Locate every blood parasite and identify its species.
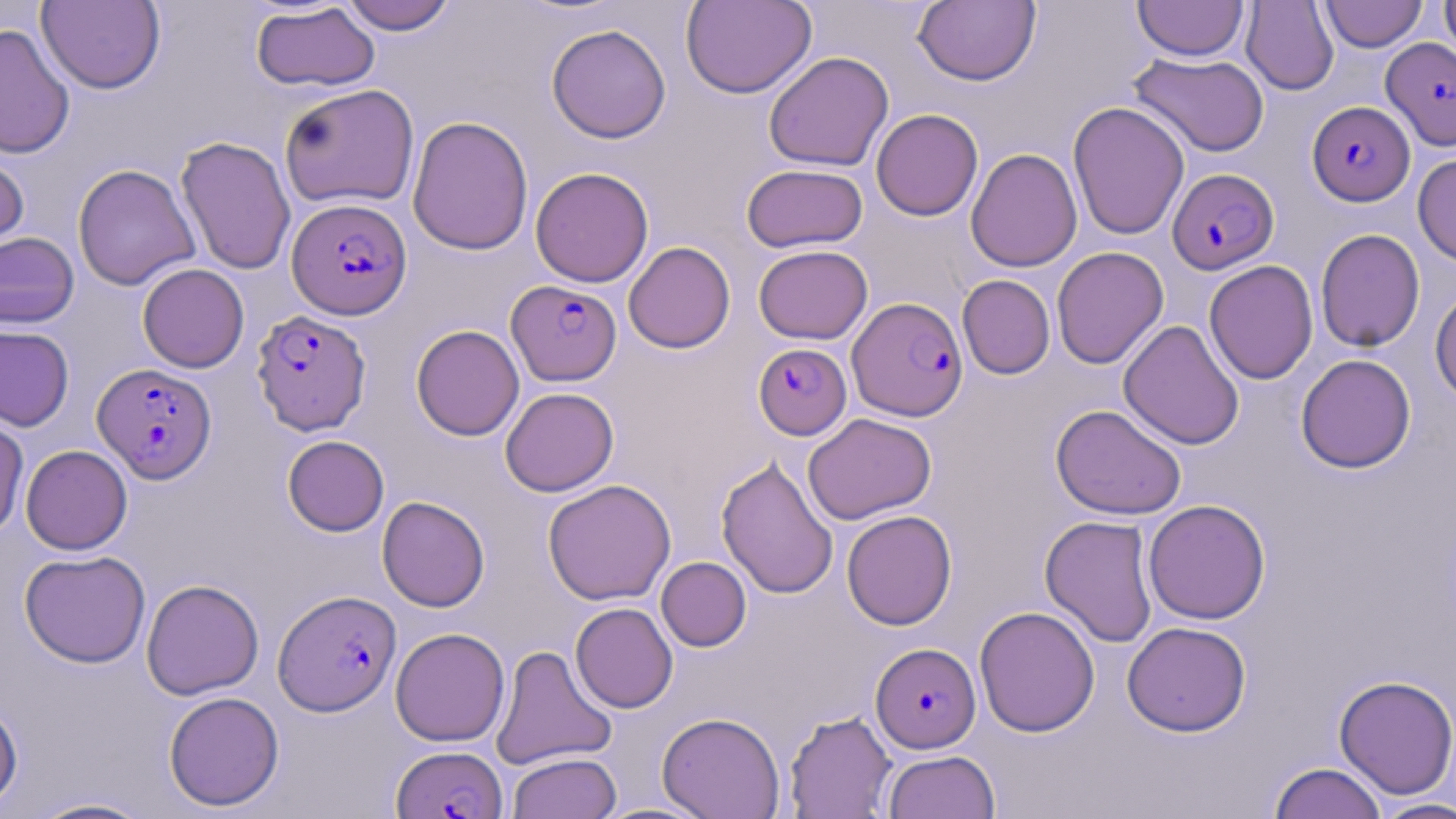
Approximate bounding boxes as named x1/y1/x2/y2 corners in pixels.
Plasmodium falciparum-infected red blood cells: (x1=1382, y1=36, x2=1456, y2=151), (x1=1307, y1=101, x2=1414, y2=206), (x1=1167, y1=168, x2=1279, y2=274), (x1=287, y1=197, x2=412, y2=320), (x1=507, y1=279, x2=621, y2=385), (x1=848, y1=297, x2=967, y2=421), (x1=251, y1=310, x2=371, y2=435), (x1=753, y1=343, x2=851, y2=439), (x1=92, y1=363, x2=216, y2=483), (x1=273, y1=589, x2=401, y2=716), (x1=870, y1=642, x2=981, y2=753), (x1=392, y1=744, x2=507, y2=819).
No Plasmodium ovale, Plasmodium malariae, Plasmodium vivax, Babesia divergens, or Trypanosoma brucei observed.

Summary:
  - Uninfected red blood cell locations: (x1=681, y1=0, x2=817, y2=99), (x1=912, y1=0, x2=1041, y2=86), (x1=1319, y1=0, x2=1427, y2=52), (x1=1440, y1=0, x2=1456, y2=65), (x1=36, y1=1, x2=165, y2=94), (x1=338, y1=1, x2=458, y2=35), (x1=1133, y1=1, x2=1249, y2=61), (x1=1240, y1=1, x2=1339, y2=95), (x1=250, y1=2, x2=380, y2=92), (x1=0, y1=23, x2=75, y2=159), (x1=546, y1=23, x2=671, y2=143), (x1=763, y1=51, x2=894, y2=172), (x1=1128, y1=52, x2=1269, y2=157), (x1=279, y1=83, x2=419, y2=209), (x1=1068, y1=101, x2=1190, y2=240), (x1=870, y1=109, x2=983, y2=221), (x1=407, y1=115, x2=533, y2=256), (x1=176, y1=136, x2=296, y2=275), (x1=966, y1=148, x2=1082, y2=272), (x1=0, y1=149, x2=30, y2=259), (x1=1413, y1=151, x2=1456, y2=267), (x1=742, y1=163, x2=868, y2=253), (x1=73, y1=164, x2=200, y2=290), (x1=530, y1=167, x2=654, y2=287), (x1=1315, y1=228, x2=1425, y2=352), (x1=0, y1=231, x2=80, y2=329), (x1=623, y1=241, x2=735, y2=354), (x1=754, y1=244, x2=873, y2=344), (x1=1051, y1=246, x2=1168, y2=369), (x1=1204, y1=260, x2=1318, y2=385), (x1=137, y1=263, x2=249, y2=373), (x1=957, y1=274, x2=1055, y2=379), (x1=1430, y1=286, x2=1456, y2=403), (x1=1118, y1=320, x2=1245, y2=450), (x1=411, y1=324, x2=524, y2=441), (x1=0, y1=325, x2=74, y2=431), (x1=1295, y1=354, x2=1416, y2=473), (x1=500, y1=387, x2=619, y2=496), (x1=1050, y1=404, x2=1187, y2=520), (x1=0, y1=413, x2=30, y2=537), (x1=803, y1=413, x2=937, y2=524), (x1=282, y1=435, x2=389, y2=536), (x1=21, y1=444, x2=132, y2=554), (x1=716, y1=456, x2=838, y2=599), (x1=543, y1=479, x2=676, y2=606), (x1=377, y1=496, x2=490, y2=612), (x1=1143, y1=499, x2=1271, y2=625), (x1=842, y1=510, x2=957, y2=630), (x1=1040, y1=515, x2=1158, y2=648), (x1=19, y1=549, x2=151, y2=668), (x1=656, y1=556, x2=751, y2=651), (x1=140, y1=578, x2=264, y2=700), (x1=570, y1=602, x2=678, y2=713), (x1=974, y1=605, x2=1100, y2=737), (x1=1122, y1=621, x2=1251, y2=737), (x1=390, y1=627, x2=510, y2=746), (x1=491, y1=645, x2=617, y2=769), (x1=1333, y1=674, x2=1456, y2=800), (x1=163, y1=691, x2=285, y2=811), (x1=0, y1=700, x2=23, y2=811), (x1=784, y1=710, x2=897, y2=818), (x1=657, y1=712, x2=786, y2=819), (x1=882, y1=749, x2=1000, y2=819), (x1=507, y1=752, x2=621, y2=819), (x1=1268, y1=762, x2=1388, y2=819), (x1=26, y1=796, x2=157, y2=818), (x1=1369, y1=798, x2=1456, y2=819), (x1=593, y1=801, x2=717, y2=818)
  - Slide-level diagnosis: Plasmodium falciparum
  - Image size: 1456×819 pixels
  - Modality: light microscopy
  - Preparation: thin blood film
  - Magnification: 1000x
  - Field of view: single
  - Stain: May-Grünwald-Giemsa